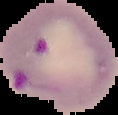 Image is 118×115 pixels. From a thin blood smear. Cell region segmented out of the field of view; the surrounding area is masked to black. Result: Plasmodium parasites detected.